Identify the cell.
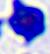

This is a leukocyte.

Photomicrograph. 400x magnification.